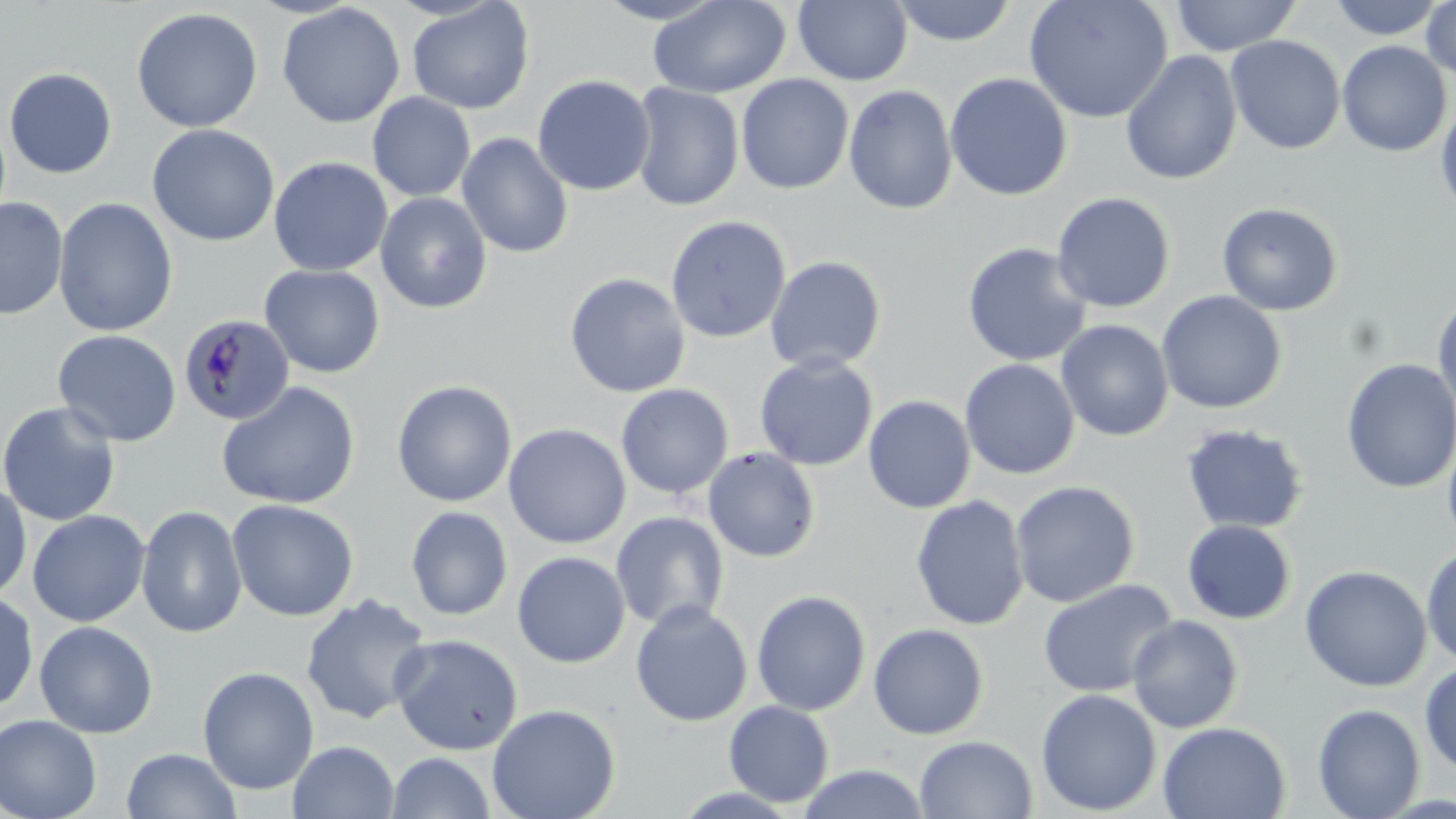

Approximate bounding boxes as (x1,y1)-(x2,y2) corner pairs in pixels. Uninfected red blood cell locations: (593,0)-(728,25), (647,0)-(793,99), (794,0)-(912,86), (890,0)-(1018,47), (1023,0)-(1173,123), (1169,0)-(1302,56), (1326,0)-(1450,41), (1421,0)-(1456,84), (406,1)-(536,114), (276,3)-(406,128), (131,7)-(264,133), (1225,35)-(1346,154), (1336,40)-(1452,157), (1120,50)-(1242,186), (3,67)-(117,179), (944,72)-(1073,201), (735,74)-(855,195), (532,75)-(656,196), (629,82)-(745,212), (843,84)-(958,215), (367,92)-(476,202), (1435,95)-(1456,220), (146,124)-(281,246), (456,133)-(574,259), (268,156)-(393,277), (375,191)-(492,313), (1051,192)-(1176,314), (0,196)-(68,320), (53,197)-(178,337), (1216,201)-(1343,316), (665,215)-(792,344), (962,242)-(1092,367), (765,256)-(887,374), (259,264)-(386,379), (564,272)-(691,398), (1156,290)-(1287,414), (1431,292)-(1456,420), (1056,319)-(1174,442), (52,329)-(182,447), (755,354)-(878,471), (1340,358)-(1455,493), (960,359)-(1081,480), (391,380)-(517,508), (216,381)-(361,509), (615,383)-(734,499), (862,395)-(976,514), (0,402)-(121,526), (503,423)-(631,550), (1180,423)-(1310,535), (1442,429)-(1456,552), (702,447)-(821,562), (1010,480)-(1141,608), (0,481)-(32,602), (910,494)-(1030,631), (226,498)-(359,622), (136,505)-(248,639), (405,505)-(514,621), (28,510)-(150,627), (611,511)-(729,630), (1182,519)-(1297,624), (1421,543)-(1456,669), (512,551)-(630,668), (1299,564)-(1433,692), (1038,579)-(1178,698), (0,590)-(39,713), (751,590)-(872,716), (300,594)-(433,725), (630,600)-(753,729), (1126,614)-(1245,733), (34,621)-(158,738), (867,623)-(989,740), (389,633)-(524,756), (1419,661)-(1456,777), (198,666)-(320,795), (1035,688)-(1162,816), (723,700)-(834,807), (487,703)-(621,819), (1312,703)-(1425,819), (0,714)-(102,819), (1157,722)-(1291,818), (913,735)-(1039,818), (288,740)-(399,819), (121,748)-(242,818), (386,752)-(496,819), (797,763)-(931,819), (666,784)-(805,818). Plasmodium malariae-infected red blood cell locations: (178,313)-(295,426). Slide-level diagnosis: Plasmodium malariae. Single field of view. Image is 1456×819 pixels. Thin blood smear. 1000x magnification. May-Grünwald-Giemsa-stained preparation. Optical microscopy.